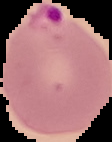

Image is 112×142 pixels. Result: malaria parasites identified. From a thin blood film. Segmented cell region on a black background.